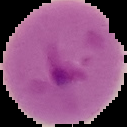 Malaria status: parasitized. Cell region segmented out of the field of view; the surrounding area is masked to black. From a thin blood film. Image is 127×127 pixels.